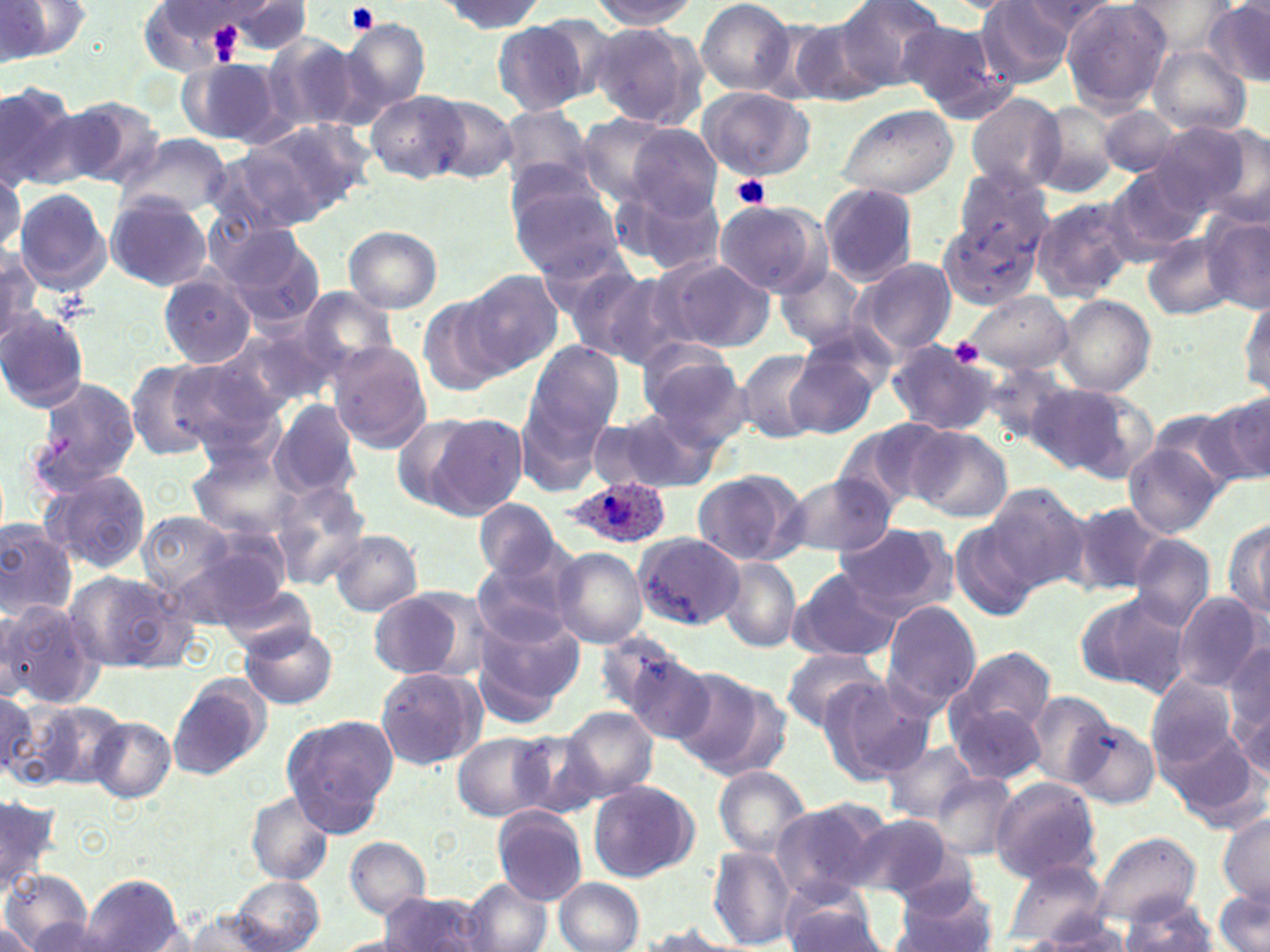

Approximate bounding boxes as [x1, y1, x2, y2] in pixels. Platelet locations: [344, 3, 381, 35], [211, 24, 239, 61], [731, 174, 771, 212], [947, 339, 987, 368]. Plasmodium ovale-infected red blood cell locations: [561, 477, 665, 550]. Uninfected red blood cell locations: [0, 0, 95, 65], [589, 0, 702, 29], [695, 0, 797, 97], [829, 0, 946, 94], [1020, 0, 1118, 37], [434, 1, 546, 33], [976, 1, 1078, 85], [1061, 1, 1173, 111], [1124, 1, 1236, 55], [144, 2, 259, 71], [223, 2, 314, 55], [1205, 2, 1270, 87], [337, 18, 430, 114], [490, 20, 591, 117], [588, 20, 706, 132], [786, 20, 889, 107], [897, 20, 1008, 116], [257, 32, 362, 139], [1148, 46, 1250, 135], [179, 56, 288, 147], [0, 82, 87, 191], [697, 86, 815, 181], [367, 92, 465, 183], [965, 92, 1065, 192], [425, 94, 519, 184], [60, 95, 164, 189], [1032, 101, 1122, 198], [835, 103, 957, 201], [1099, 106, 1187, 177], [498, 107, 596, 190], [623, 108, 789, 209], [574, 116, 678, 202], [245, 119, 372, 223], [1147, 120, 1259, 219], [626, 126, 723, 221], [117, 131, 231, 217], [204, 147, 325, 240], [954, 167, 1053, 257], [1105, 167, 1209, 262], [0, 172, 23, 266], [507, 176, 624, 278], [819, 183, 919, 285], [613, 184, 727, 278], [13, 186, 114, 295], [105, 193, 213, 292], [1031, 196, 1138, 300], [711, 201, 827, 297], [940, 214, 1054, 317], [1203, 216, 1270, 315], [343, 226, 442, 312], [228, 229, 324, 332], [1143, 231, 1240, 322], [0, 248, 44, 344], [539, 249, 652, 349], [659, 258, 775, 353], [850, 258, 955, 357], [775, 264, 871, 354], [462, 268, 564, 375], [569, 271, 680, 368], [159, 272, 259, 367], [291, 285, 399, 382], [960, 291, 1072, 374], [1240, 294, 1269, 400], [1055, 295, 1156, 396], [417, 297, 513, 396], [0, 309, 92, 413], [215, 326, 333, 415], [885, 340, 998, 437], [524, 341, 626, 441], [328, 342, 433, 453], [785, 343, 883, 438], [638, 345, 749, 444], [733, 348, 827, 443], [169, 359, 287, 457], [979, 360, 1071, 447], [125, 361, 223, 462], [25, 376, 140, 496], [1027, 382, 1151, 481], [517, 394, 612, 494], [1204, 395, 1270, 489], [268, 401, 361, 500], [590, 409, 718, 494], [390, 412, 490, 514], [428, 412, 529, 519], [833, 417, 953, 514], [906, 427, 1012, 523], [1124, 442, 1223, 537], [185, 443, 300, 543], [691, 468, 809, 567], [40, 469, 153, 576], [780, 473, 897, 558], [267, 479, 372, 588], [985, 482, 1088, 589], [473, 498, 560, 583], [1064, 500, 1169, 596], [138, 511, 239, 601], [1223, 515, 1269, 625], [949, 520, 1041, 622], [0, 521, 78, 619], [833, 521, 955, 618], [330, 529, 423, 616], [634, 533, 743, 629], [1129, 535, 1214, 632], [549, 546, 648, 648], [472, 550, 579, 645], [721, 556, 801, 651], [787, 566, 902, 663], [62, 569, 196, 675], [218, 581, 319, 658], [367, 587, 480, 682], [1075, 592, 1190, 696], [1173, 593, 1265, 693], [0, 599, 105, 709], [882, 600, 982, 712], [473, 616, 582, 726], [240, 624, 340, 708], [599, 632, 701, 731], [1226, 643, 1270, 771], [951, 645, 1057, 748], [780, 646, 884, 734], [621, 652, 730, 749], [374, 666, 485, 772], [669, 668, 779, 773], [1149, 673, 1246, 776], [168, 674, 270, 779], [819, 676, 932, 785], [1, 690, 43, 784], [1023, 692, 1114, 786], [946, 695, 1049, 787], [17, 698, 129, 791], [563, 705, 660, 802], [1064, 714, 1160, 810], [88, 715, 177, 804], [283, 717, 397, 834], [1155, 718, 1262, 828], [512, 730, 605, 819], [453, 733, 551, 820], [880, 738, 979, 823], [713, 765, 812, 858], [929, 772, 1020, 861], [989, 776, 1103, 882], [586, 779, 698, 882], [244, 791, 334, 885], [1, 793, 59, 892], [768, 796, 894, 901], [491, 805, 588, 904], [846, 812, 957, 900], [1217, 813, 1270, 906], [1091, 830, 1200, 927], [344, 836, 431, 920], [707, 846, 796, 949], [1004, 859, 1110, 943], [0, 871, 93, 952], [77, 876, 187, 952], [229, 876, 324, 950], [463, 878, 551, 952], [554, 878, 644, 951], [891, 880, 999, 952], [777, 883, 887, 952], [1214, 890, 1269, 952], [379, 891, 489, 950], [1120, 895, 1218, 952], [1017, 898, 1136, 945], [180, 910, 274, 952], [0, 921, 40, 950], [631, 923, 741, 952]. Slide-level diagnosis: Plasmodium ovale. Thin blood film. Light microscopy. 1000x magnification. One field of a larger specimen. May-Grünwald-Giemsa stain. Image is 1270×952 pixels.